Describe the morphology of the red blood cells.
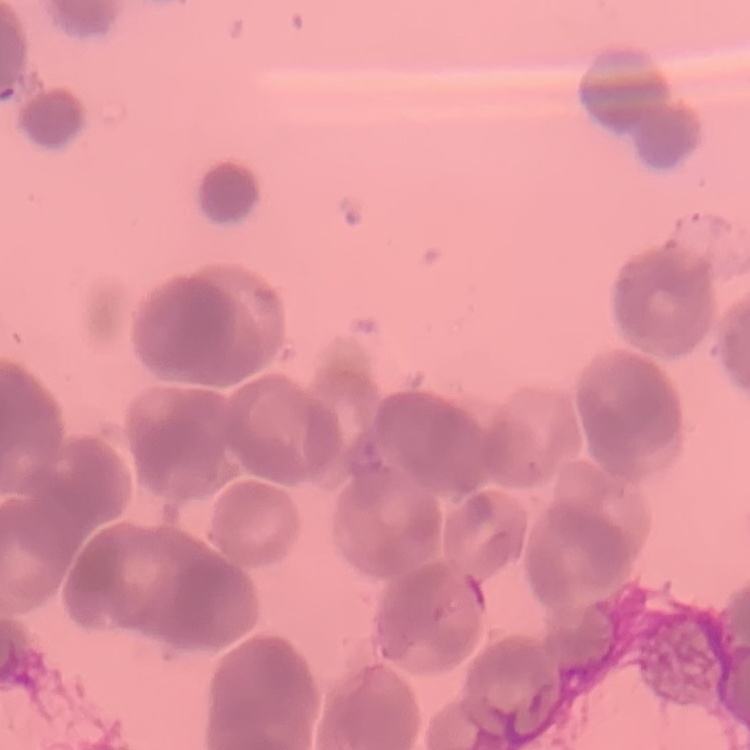
Rouleaux formation.

One tile cut from a larger photomicrograph. Thin blood smear. Stained with either Field's or Giemsa.